Assess for malaria.
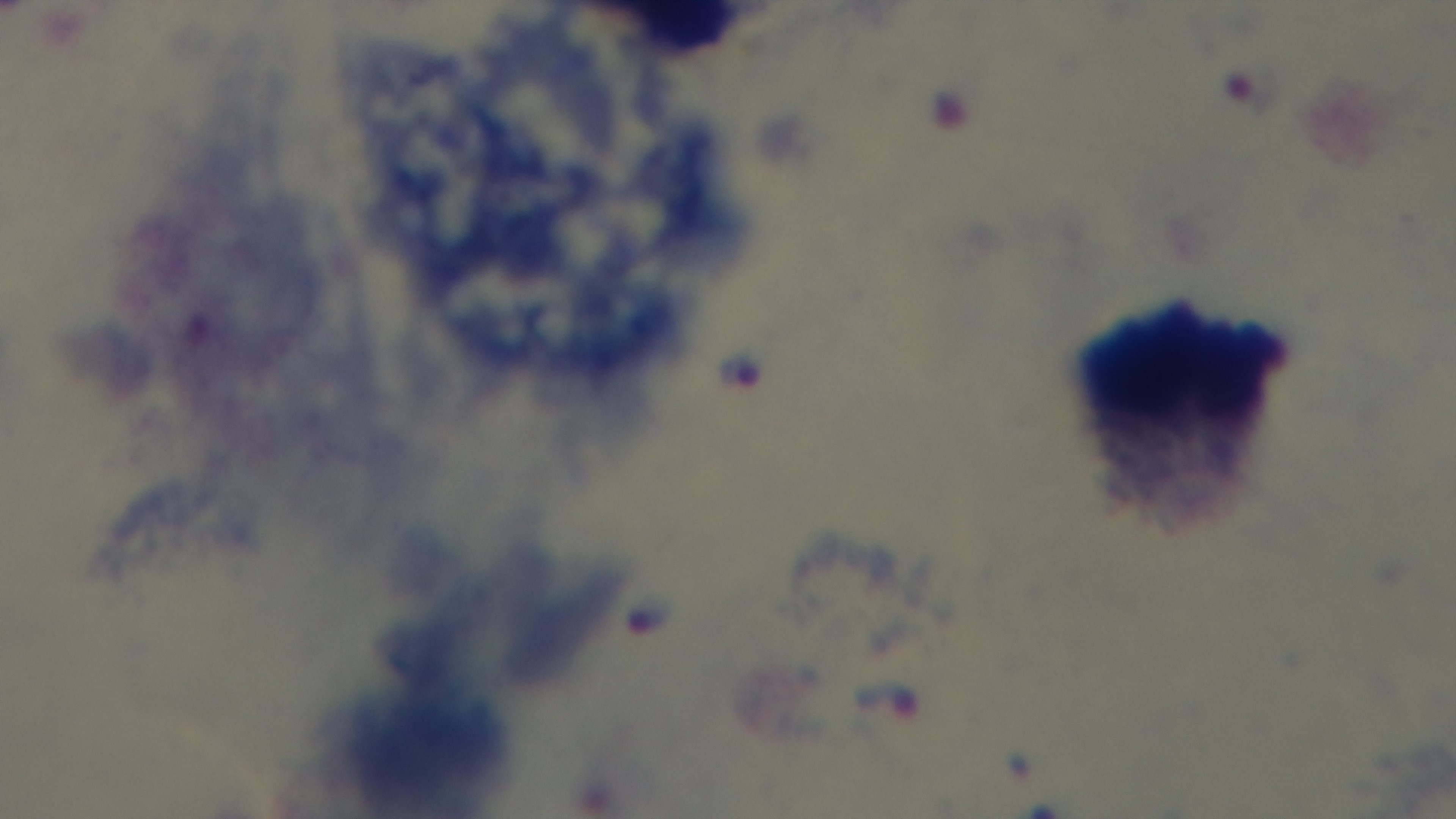

Infected.

capture = mounted 4K digital camera
preparation = thick smear
modality = light microscopy
stain = Giemsa
field of view = single
objective = 100x oil immersion